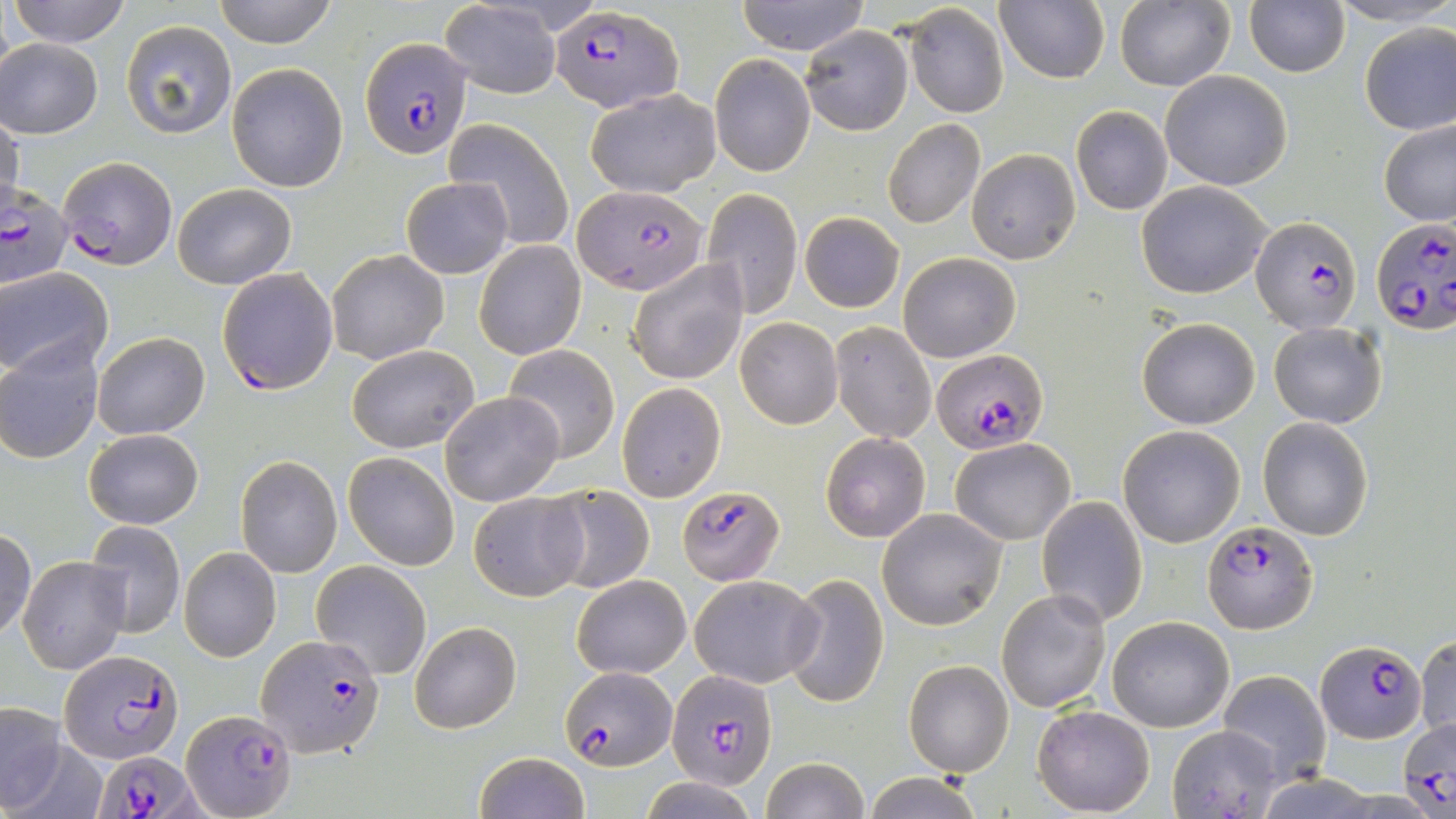
slide-level diagnosis = Plasmodium falciparum
magnification = 1000x
field of view = single
uninfected red blood cell locations = approximate bounding boxes as [x1, y1, x2, y2] in pixels: [10, 0, 132, 46], [212, 0, 338, 49], [734, 0, 870, 54], [994, 0, 1108, 86], [1114, 0, 1235, 92], [1244, 0, 1351, 77], [1326, 1, 1456, 26], [440, 2, 561, 97], [904, 4, 1009, 119], [120, 19, 237, 139], [1358, 22, 1456, 136], [800, 25, 913, 135], [1, 37, 102, 139], [709, 55, 814, 177], [226, 62, 348, 193], [1159, 70, 1293, 190], [585, 87, 720, 199], [1070, 104, 1173, 215], [0, 112, 23, 222], [446, 117, 575, 251], [882, 118, 985, 231], [1379, 118, 1456, 228], [966, 148, 1079, 264], [401, 177, 513, 277], [1136, 181, 1274, 299], [174, 183, 295, 290], [702, 187, 802, 319], [800, 212, 904, 312], [475, 239, 586, 359], [326, 249, 450, 364], [897, 250, 1019, 362], [626, 258, 747, 385], [2, 268, 115, 379], [1137, 316, 1262, 428], [735, 317, 841, 428], [828, 321, 937, 444], [1269, 321, 1386, 427], [92, 331, 210, 440], [0, 341, 104, 464], [346, 345, 478, 453], [502, 345, 621, 464], [617, 383, 726, 501], [440, 391, 565, 506], [1257, 416, 1374, 541], [1118, 424, 1245, 547], [83, 428, 203, 530], [820, 431, 931, 543], [951, 436, 1075, 546], [343, 452, 460, 571], [235, 456, 342, 577], [544, 484, 654, 595], [467, 490, 588, 601], [1037, 495, 1148, 627], [877, 508, 1007, 630], [83, 520, 186, 639], [0, 527, 37, 641], [173, 545, 279, 661], [19, 556, 129, 675], [310, 560, 432, 680], [781, 572, 890, 708], [572, 574, 690, 679], [690, 574, 824, 688], [996, 588, 1111, 713], [1107, 616, 1235, 732], [410, 619, 522, 734], [1415, 634, 1456, 742], [903, 659, 1013, 776], [1218, 670, 1332, 784], [0, 703, 70, 813], [1032, 704, 1155, 816], [1167, 723, 1286, 819], [473, 750, 590, 819], [758, 756, 869, 819], [861, 772, 987, 818], [640, 778, 757, 817]
modality = optical microscopy
image size = 1456×819 pixels
Plasmodium falciparum-infected red blood cell locations = approximate bounding boxes as [x1, y1, x2, y2] in pixels: [552, 4, 680, 113], [362, 37, 471, 160], [57, 157, 177, 270], [0, 184, 74, 289], [573, 186, 706, 294], [1371, 216, 1456, 333], [1250, 217, 1362, 333], [216, 266, 341, 395], [933, 349, 1047, 451], [675, 485, 783, 584], [1202, 519, 1317, 633], [256, 635, 385, 756], [1316, 640, 1425, 743], [59, 648, 184, 764], [558, 667, 676, 770], [665, 667, 776, 789], [181, 710, 294, 818], [1397, 715, 1456, 815], [94, 747, 202, 819]
stain = May-Grünwald-Giemsa
preparation = thin blood film